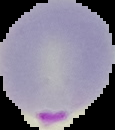 Cell region segmented out of the field of view; the surrounding area is masked to black. Result: malaria parasites identified. Image is 115×130 pixels. From a thin blood film.